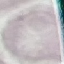
result = no malaria parasites seen
stain = Giemsa
preparation = thin smear
capture = smartphone through the microscope eyepiece
image type = automatically extracted cell patch, resized to 64 × 64 pixels